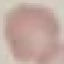 Malaria status: uninfected. Thin blood smear. Acquired by smartphone through the microscope eyepiece. Giemsa stain. Cell patch, automatically extracted from a larger field of view and resized to 64 × 64 pixels.